Locate and identify every blood parasite.
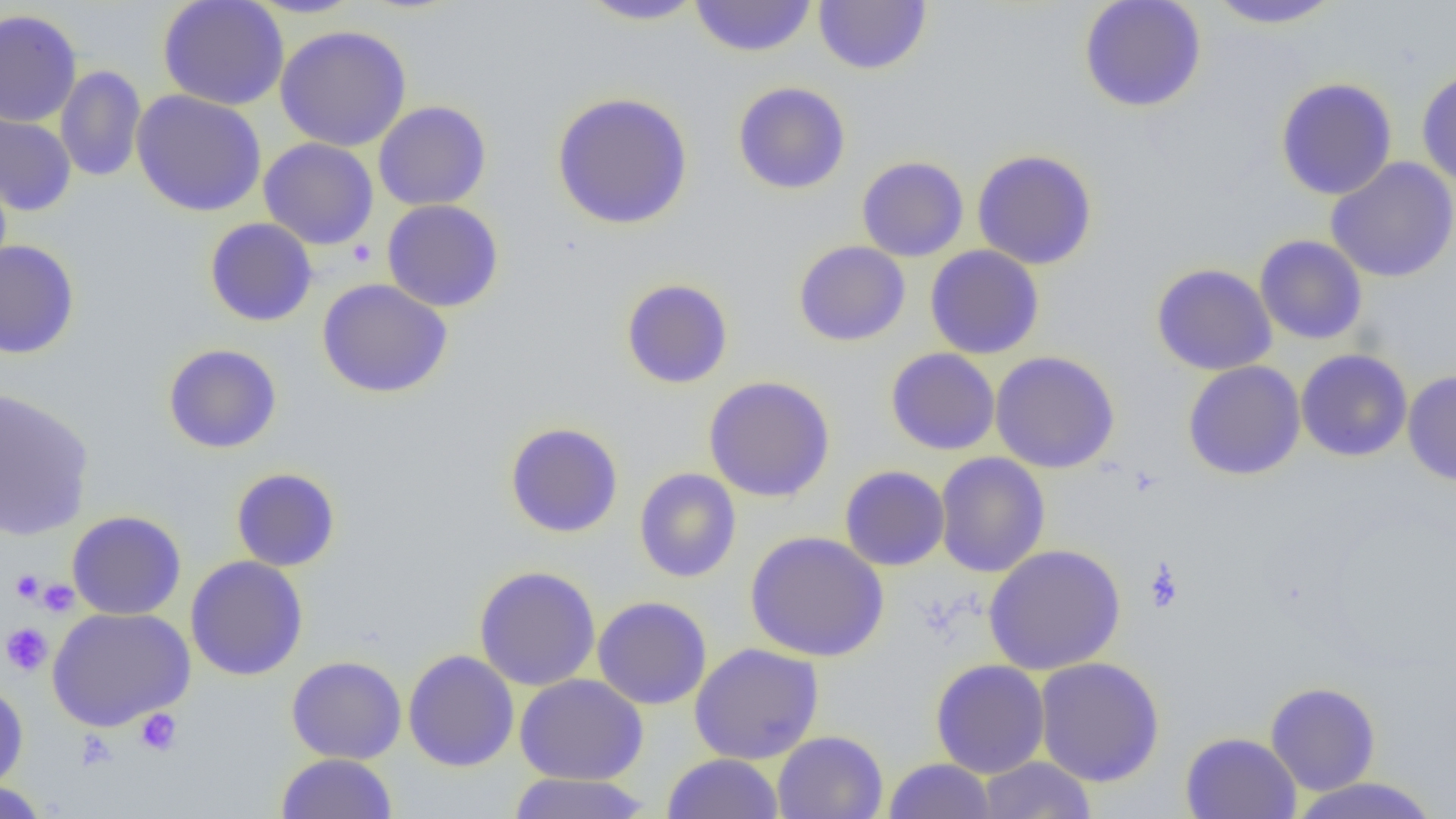

No blood parasites seen.

slide-level diagnosis = no evidence of blood parasites
image size = 1456×819 pixels
field of view = one of a larger specimen
uninfected red blood cell locations = approximate bounding boxes as (x1,y1)-(x2,y2) corner pairs in pixels: (157,0)-(289,111), (244,0)-(366,19), (577,0)-(709,25), (689,0)-(817,57), (1078,0)-(1207,113), (1205,0)-(1344,30), (813,1)-(932,74), (0,9)-(82,127), (275,25)-(412,152), (55,65)-(146,182), (1416,68)-(1456,187), (1275,77)-(1397,200), (732,81)-(851,195), (131,90)-(267,216), (552,91)-(694,230), (373,101)-(491,211), (0,109)-(77,217), (258,138)-(379,250), (972,149)-(1098,270), (856,156)-(969,261), (1325,157)-(1456,283), (382,199)-(504,312), (204,218)-(318,326), (1254,235)-(1368,344), (0,239)-(80,359), (793,240)-(910,346), (925,245)-(1044,359), (1151,263)-(1277,375), (317,278)-(453,398), (620,278)-(733,389), (162,343)-(282,454), (885,348)-(1000,455), (1296,349)-(1412,462), (990,350)-(1120,473), (1182,360)-(1306,480), (1403,370)-(1456,486), (703,376)-(835,502), (0,387)-(95,541), (504,422)-(624,538), (934,451)-(1050,578), (839,465)-(950,571), (230,467)-(341,572), (634,468)-(741,583), (67,510)-(186,620), (745,530)-(889,662), (983,543)-(1126,674), (185,556)-(308,680), (474,565)-(600,691), (592,595)-(712,710), (47,607)-(195,731), (689,642)-(824,764), (403,650)-(520,772), (286,655)-(407,764), (1035,656)-(1165,787), (931,659)-(1050,778), (514,674)-(648,785), (0,681)-(29,793), (1265,682)-(1381,795), (772,730)-(888,819), (1180,731)-(1301,819), (276,752)-(398,819), (663,753)-(784,819), (976,756)-(1097,818), (883,758)-(996,818), (508,772)-(652,818), (1288,776)-(1441,818), (0,781)-(51,818)
platelet locations = approximate bounding boxes as (x1,y1)-(x2,y2) corner pairs in pixels: (346,239)-(377,267), (1143,560)-(1185,612), (10,569)-(44,604), (37,578)-(79,617), (1,622)-(53,676), (135,709)-(182,757), (77,730)-(118,771)
magnification = 1000x
preparation = thin blood film
modality = optical microscopy